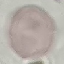

malaria status = uninfected
image type = automatically extracted cell patch, resized to 64 × 64 pixels
stain = Giemsa
capture = smartphone camera at the microscope eyepiece
preparation = thin smear